Give the extent of all Trypanosoma brucei.
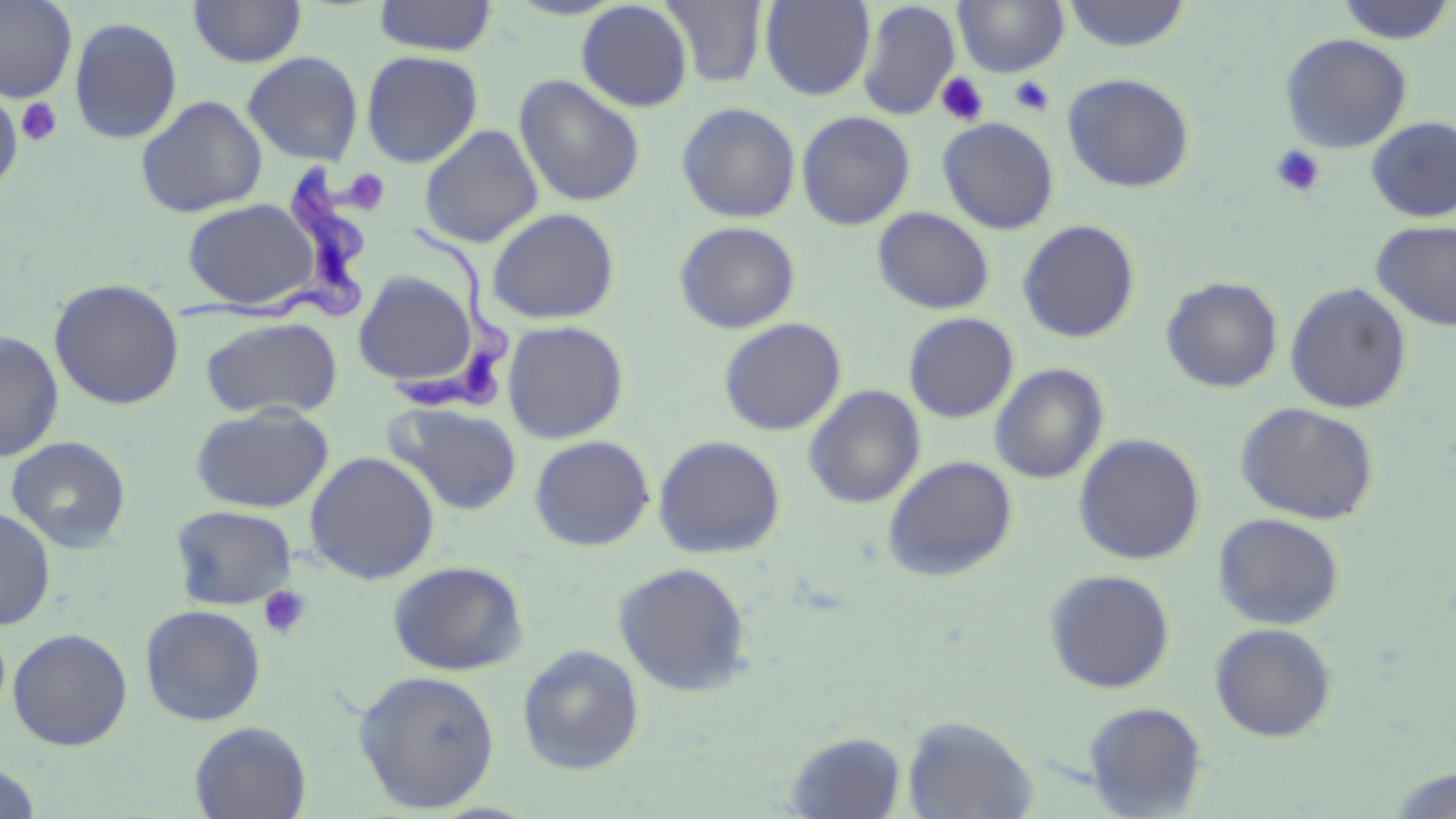

Approximate bounding boxes as (x1, y1, x2, y2) in pixels.
Trypanosoma brucei: (169, 161, 371, 333), (394, 214, 514, 413).

Platelet locations: (936, 72, 990, 126), (1010, 76, 1055, 116), (16, 98, 63, 147), (1270, 144, 1326, 196), (345, 167, 386, 211), (257, 585, 312, 641). Uninfected red blood cell locations: (0, 0, 77, 103), (188, 0, 307, 68), (372, 0, 498, 56), (660, 0, 769, 88), (760, 0, 875, 101), (1337, 0, 1455, 45), (576, 1, 694, 112), (857, 1, 960, 120), (954, 1, 1069, 77), (1062, 1, 1193, 52), (68, 17, 183, 144), (1279, 33, 1413, 153), (360, 50, 483, 168), (242, 51, 364, 166), (1062, 73, 1195, 193), (514, 74, 646, 208), (0, 89, 23, 195), (135, 95, 268, 217), (677, 102, 801, 223), (797, 111, 916, 230), (1366, 116, 1456, 222), (938, 117, 1059, 235), (420, 125, 544, 248), (182, 198, 322, 310), (872, 207, 995, 314), (487, 208, 621, 325), (1017, 219, 1141, 343), (674, 221, 800, 334), (1371, 221, 1456, 331), (352, 270, 480, 391), (1161, 276, 1283, 393), (48, 278, 185, 410), (1284, 283, 1413, 414), (903, 312, 1019, 423), (200, 316, 343, 420), (718, 318, 846, 436), (502, 320, 629, 444), (0, 331, 64, 462), (990, 363, 1109, 484), (804, 385, 925, 509), (386, 402, 523, 515), (1236, 402, 1379, 525), (190, 405, 333, 513), (1074, 433, 1206, 565), (530, 435, 654, 551), (653, 435, 786, 559), (5, 436, 132, 553), (304, 451, 440, 585), (883, 455, 1018, 581), (170, 505, 298, 610), (0, 507, 56, 630), (1213, 513, 1344, 630), (387, 560, 529, 676), (613, 561, 754, 696), (1044, 569, 1176, 693), (140, 604, 266, 726), (1209, 622, 1337, 742), (7, 627, 132, 751), (516, 644, 645, 775), (353, 669, 501, 812), (1083, 701, 1208, 817), (902, 716, 1038, 818), (189, 721, 312, 819), (785, 731, 908, 818), (0, 762, 43, 818), (1385, 767, 1456, 817). Slide-level diagnosis: Trypanosoma brucei. Optical microscopy. Thin blood smear. Captured at 1000x magnification. May-Grünwald-Giemsa stain. Image is 1456×819 pixels. One field of a larger specimen.